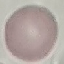

Summary:
  - Result: no malaria parasites seen
  - Stain: Giemsa
  - Capture: smartphone camera at the microscope eyepiece
  - Image type: automatically extracted cell patch, resized to 64 × 64 pixels
  - Preparation: thin smear